Locate and identify every blood parasite.
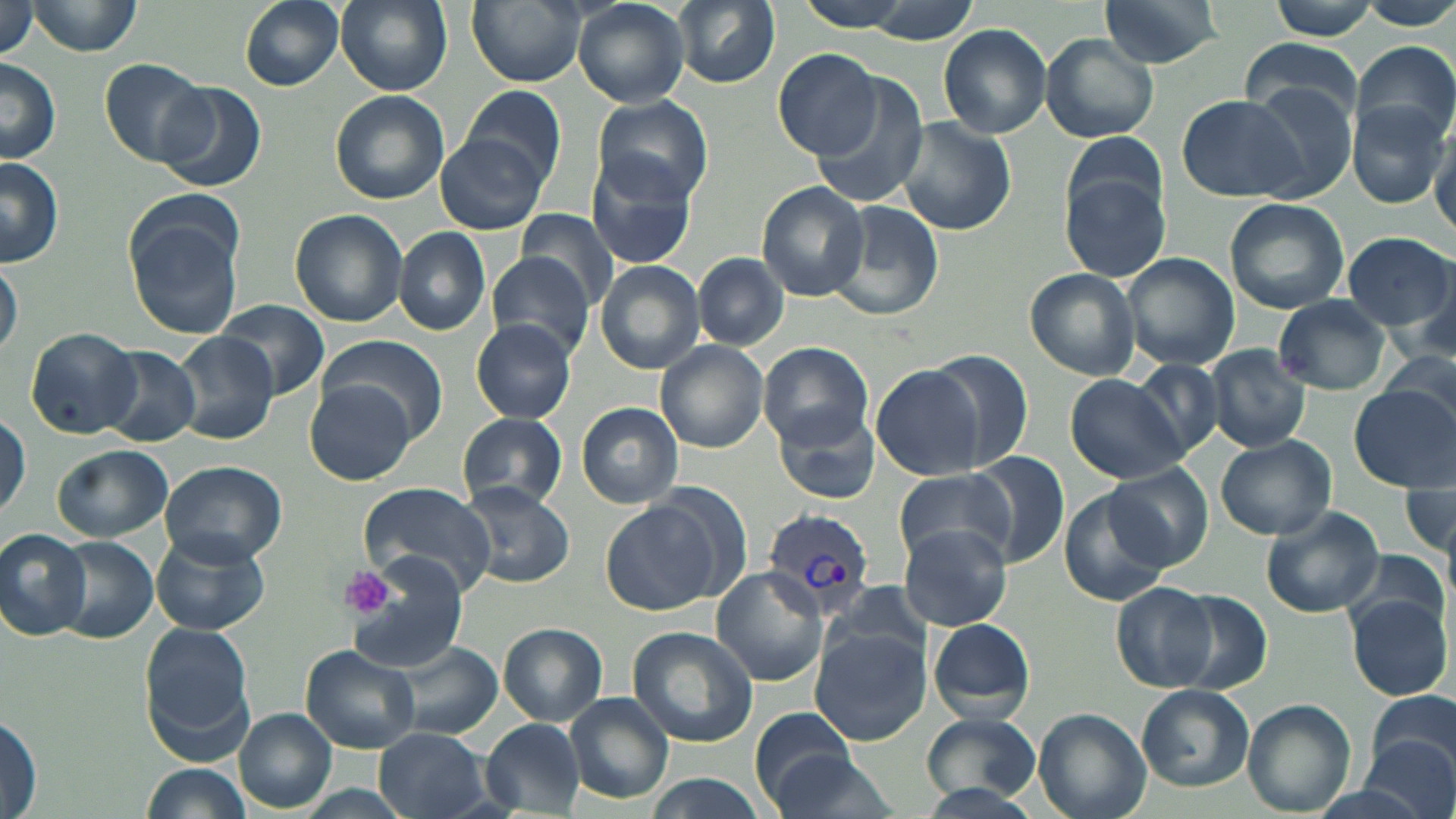

Approximate bounding boxes as (x1, y1, x2, y2) in pixels.
Plasmodium vivax-infected red blood cells: (761, 511, 876, 616).
No Plasmodium falciparum, Plasmodium ovale, Plasmodium malariae, Babesia divergens, or Trypanosoma brucei observed.

Platelet locations: (338, 567, 399, 622). Uninfected red blood cell locations: (22, 0, 144, 56), (238, 0, 344, 90), (335, 0, 452, 95), (467, 0, 586, 87), (572, 0, 690, 108), (672, 0, 781, 88), (794, 0, 917, 32), (1095, 0, 1226, 70), (1268, 0, 1383, 40), (858, 1, 983, 42), (0, 2, 38, 61), (939, 24, 1052, 139), (1038, 34, 1159, 144), (1239, 41, 1364, 134), (1351, 41, 1455, 148), (773, 48, 881, 159), (100, 58, 210, 166), (0, 59, 63, 163), (810, 81, 931, 207), (153, 82, 266, 194), (1245, 84, 1357, 203), (461, 85, 569, 186), (330, 90, 448, 205), (1176, 93, 1314, 205), (592, 94, 714, 205), (1349, 102, 1449, 209), (895, 116, 1016, 238), (1430, 124, 1456, 237), (1062, 130, 1170, 235), (435, 133, 551, 235), (585, 151, 700, 270), (0, 159, 65, 267), (1061, 175, 1169, 283), (758, 182, 871, 300), (1225, 198, 1350, 314), (829, 201, 945, 322), (124, 203, 246, 340), (290, 209, 408, 326), (517, 209, 619, 308), (393, 227, 491, 336), (1343, 232, 1454, 333), (694, 252, 789, 349), (1122, 253, 1238, 369), (487, 254, 593, 356), (1, 260, 22, 359), (595, 260, 704, 373), (1025, 267, 1140, 383), (1272, 295, 1393, 396), (216, 299, 329, 398), (470, 319, 576, 422), (25, 328, 140, 438), (168, 331, 280, 445), (315, 334, 447, 439), (655, 340, 770, 453), (759, 340, 873, 448), (99, 345, 202, 447), (1204, 345, 1312, 453), (920, 349, 1035, 470), (1376, 352, 1456, 430), (1130, 361, 1224, 457), (870, 365, 986, 480), (1064, 374, 1192, 483), (305, 383, 416, 484), (1346, 383, 1456, 492), (577, 402, 683, 507), (773, 403, 883, 506), (1, 411, 30, 519), (458, 413, 569, 510), (1214, 435, 1337, 540), (51, 444, 174, 541), (964, 450, 1070, 570), (157, 459, 287, 566), (1109, 465, 1211, 570), (1398, 468, 1455, 566), (892, 470, 1013, 565), (358, 481, 496, 596), (457, 483, 576, 588), (1058, 488, 1173, 607), (600, 498, 723, 615), (1259, 506, 1385, 618), (896, 522, 1015, 632), (1, 529, 89, 639), (151, 532, 267, 635), (54, 538, 159, 642), (1343, 546, 1449, 644), (341, 552, 470, 684), (712, 564, 831, 687), (820, 580, 937, 670), (1111, 582, 1218, 693), (1173, 589, 1273, 692), (1346, 595, 1452, 702), (927, 616, 1037, 721), (139, 623, 256, 756), (500, 623, 606, 724), (627, 627, 759, 748), (809, 629, 932, 744), (380, 640, 505, 742), (301, 645, 420, 755), (1135, 684, 1254, 792), (1369, 689, 1455, 778), (565, 692, 675, 805), (1244, 698, 1356, 817), (751, 707, 862, 809), (1034, 708, 1151, 819), (235, 709, 336, 811), (1, 711, 43, 816), (921, 712, 1043, 804), (481, 719, 585, 812), (376, 729, 487, 819), (1360, 732, 1454, 819), (763, 746, 901, 819), (142, 763, 252, 818), (645, 774, 769, 819), (911, 783, 1046, 819). Slide-level diagnosis: Plasmodium vivax. Optical microscopy. One field of a larger specimen. Captured at 1000x magnification. May-Grünwald-Giemsa-stained preparation. Image is 1456×819 pixels. Thin blood film.